Identify the cell.
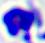
This is a leukocyte.

{
  "modality": "micrograph",
  "magnification": "400x"
}